Outline each Plasmodium falciparum-infected red blood cell.
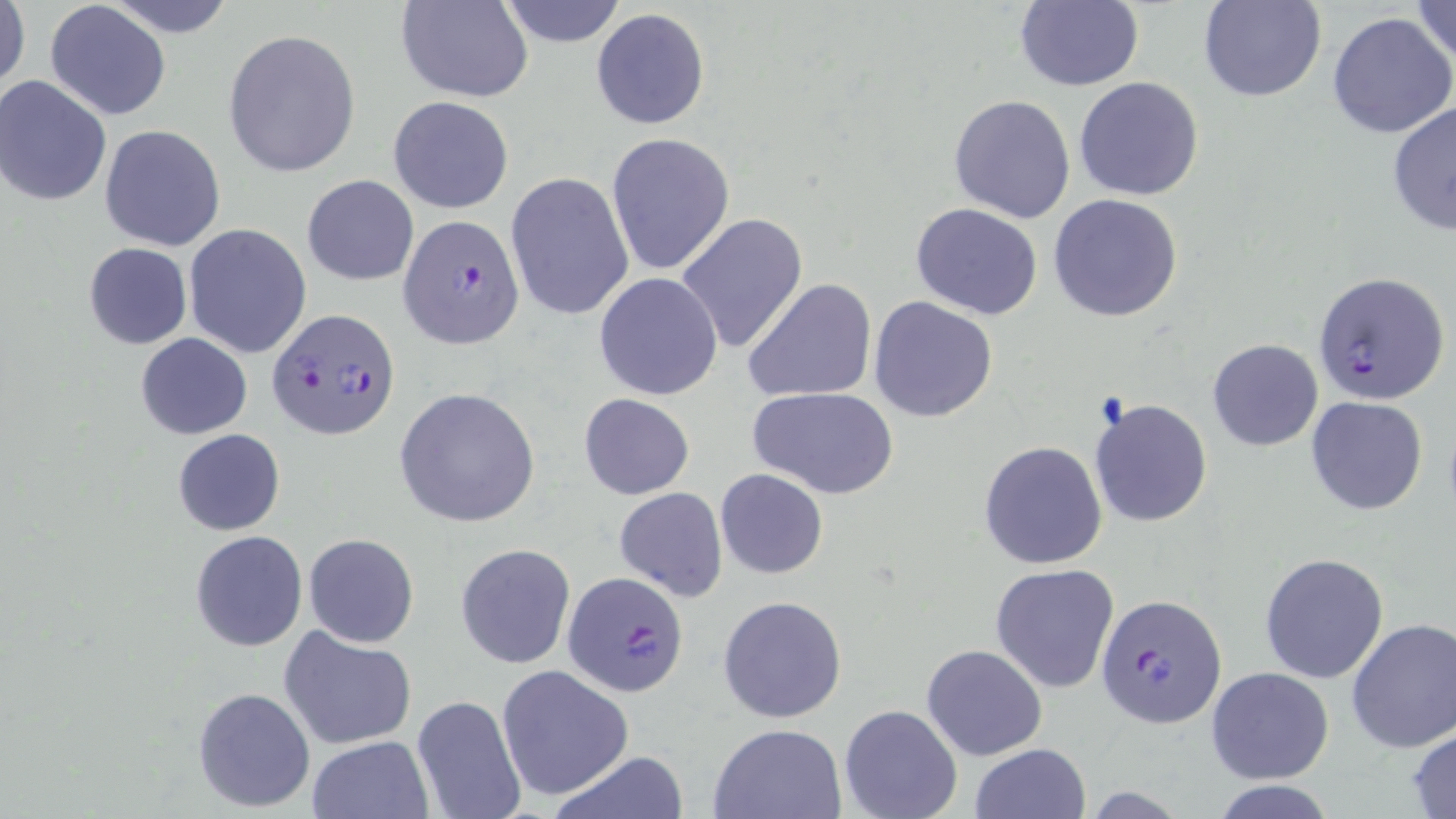

Approximate bounding boxes as [x1, y1, x2, y2] in pixels.
Plasmodium falciparum-infected red blood cells: [398, 214, 524, 349], [1313, 270, 1450, 406], [269, 307, 400, 439], [561, 573, 689, 697], [1095, 594, 1227, 728].

Summary:
  - Uninfected red blood cell locations: [1, 0, 29, 99], [104, 0, 240, 37], [396, 0, 534, 101], [496, 0, 629, 48], [1014, 0, 1144, 91], [1197, 0, 1327, 103], [1407, 0, 1456, 68], [44, 2, 172, 122], [590, 7, 711, 129], [1327, 10, 1456, 140], [222, 28, 362, 178], [0, 75, 114, 208], [1074, 77, 1205, 202], [388, 95, 513, 213], [949, 95, 1077, 224], [1386, 99, 1456, 236], [99, 126, 225, 251], [606, 132, 735, 276], [506, 172, 635, 321], [302, 175, 419, 286], [1049, 193, 1183, 322], [910, 202, 1043, 319], [675, 213, 807, 355], [185, 224, 312, 359], [83, 243, 192, 350], [593, 272, 723, 401], [744, 278, 877, 404], [869, 297, 999, 422], [134, 334, 253, 440], [1208, 338, 1324, 451], [394, 386, 541, 527], [749, 386, 899, 499], [578, 393, 694, 499], [1306, 395, 1430, 516], [1088, 397, 1213, 528], [172, 429, 287, 536], [977, 441, 1108, 569], [715, 468, 828, 579], [613, 488, 727, 603], [189, 529, 308, 652], [304, 534, 420, 648], [455, 543, 576, 669], [1260, 553, 1388, 684], [991, 563, 1119, 692], [718, 595, 848, 724], [1345, 617, 1456, 753], [280, 628, 418, 749], [922, 643, 1047, 761], [496, 665, 633, 799], [1206, 666, 1334, 783], [191, 686, 316, 813], [411, 694, 527, 819], [839, 703, 963, 819], [707, 723, 847, 818], [1407, 726, 1456, 818], [306, 734, 433, 819], [970, 743, 1091, 819], [546, 750, 692, 819]
  - Slide-level diagnosis: Plasmodium falciparum
  - Stain: May-Grünwald-Giemsa
  - Modality: light microscopy
  - Preparation: thin blood film
  - Image size: 1456×819 pixels
  - Field of view: one of a larger specimen
  - Magnification: 1000x